Locate every leukocyte (white blood cell).
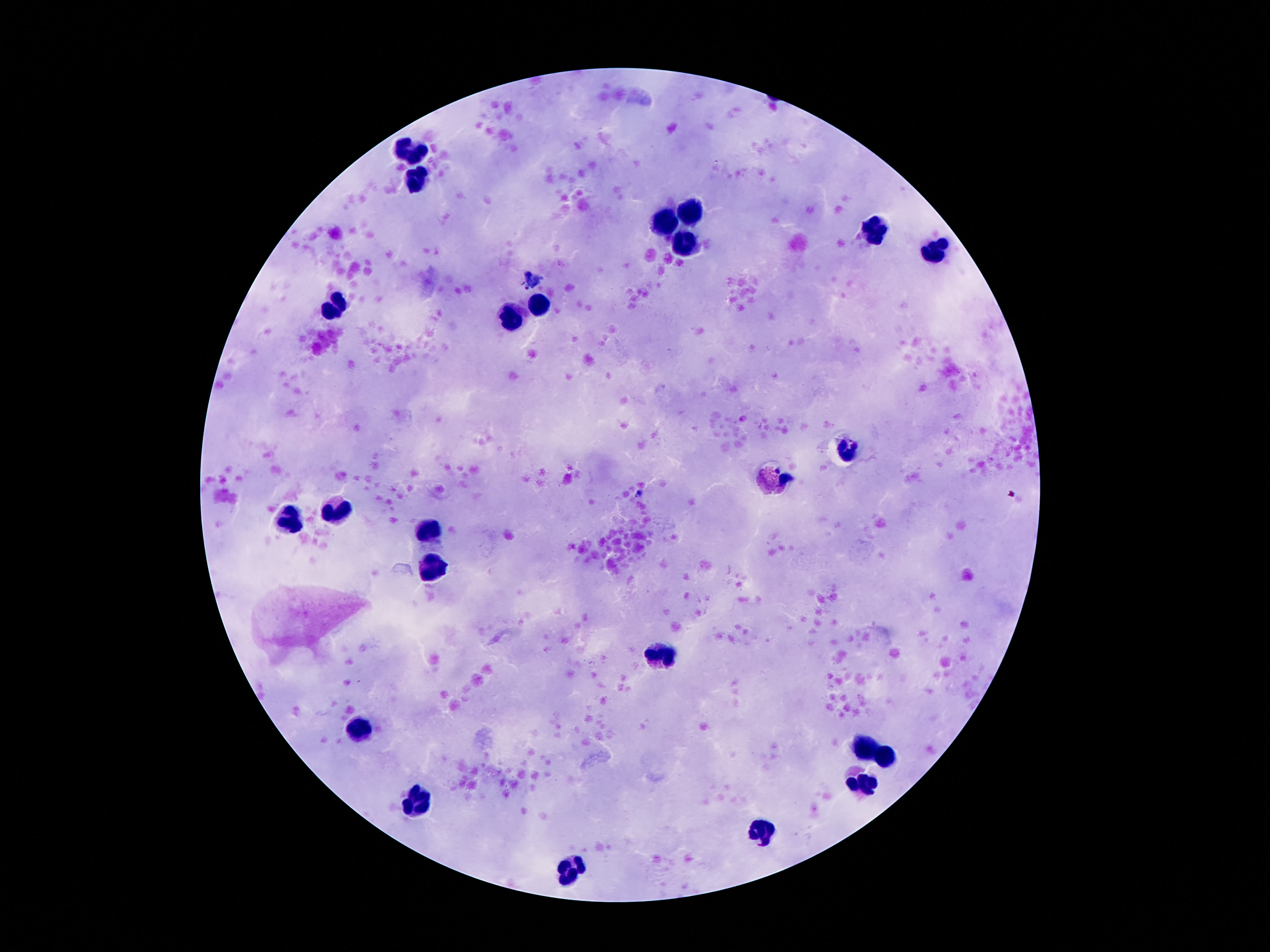

Approximate centers as {x, y} in pixels.
Leukocytes: {410, 152}, {414, 179}, {692, 215}, {668, 224}, {873, 229}, {688, 246}, {936, 246}, {539, 305}, {338, 307}, {514, 316}, {848, 449}, {774, 477}, {334, 508}, {287, 519}, {430, 531}, {434, 566}, {660, 655}, {360, 725}, {864, 749}, {889, 758}, {864, 782}, {420, 805}, {760, 833}, {569, 874}.

Summary:
  - Preparation: thick peripheral-blood smear
  - Field of view: single
  - Image size: 1270×952 pixels
  - Magnification: 100x
  - Patient malaria status: not infected
  - Capture: smartphone camera through the microscope eyepiece
  - Stain: Giemsa